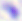
Captured at 400x magnification. Micrograph. Toxoplasma gondii is shown.